Locate every Trypanosoma brucei.
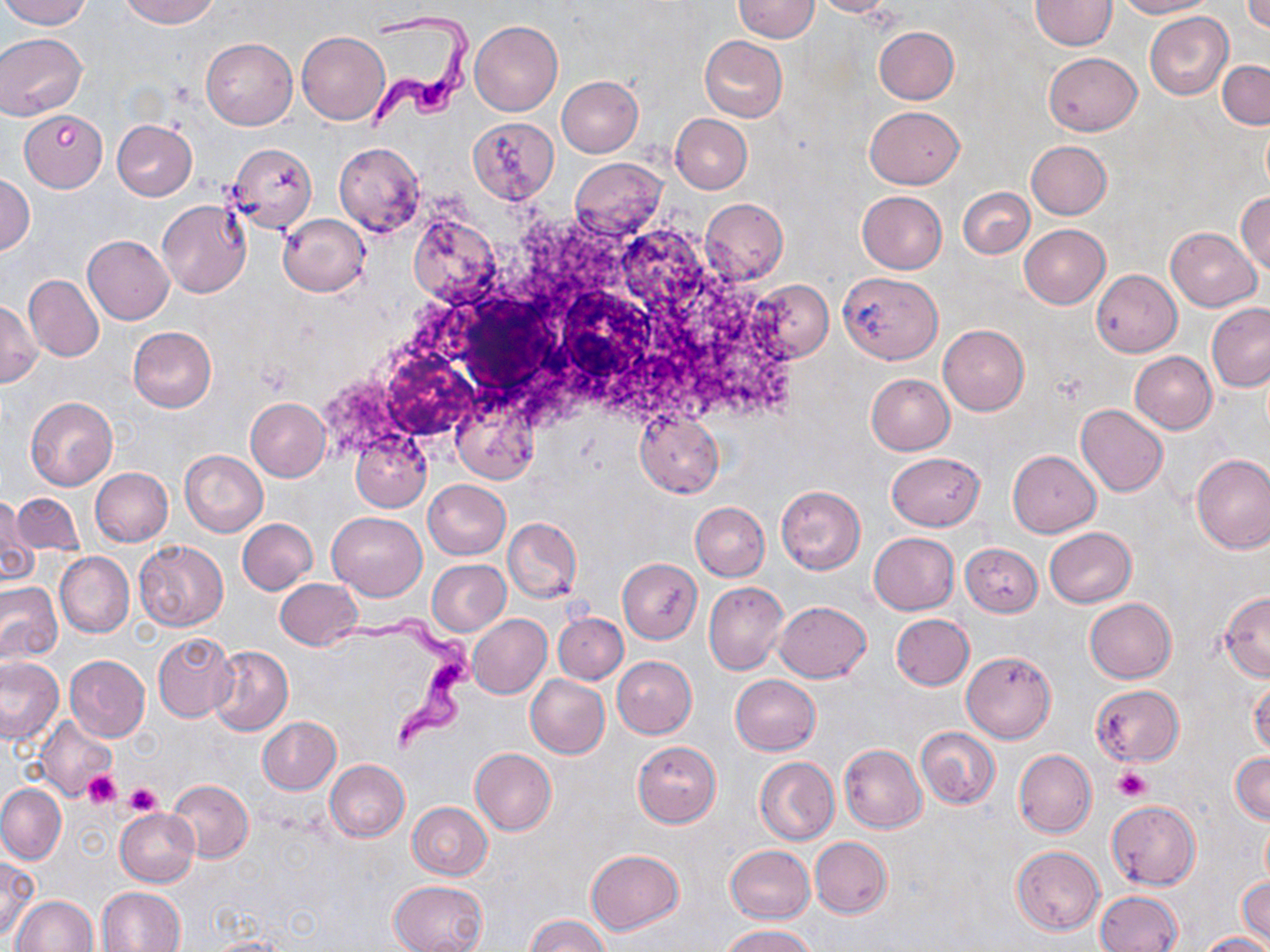

Approximate bounding boxes as (x1,y1)-(x2,y2) corner pairs in pixels.
Trypanosoma brucei: (362,12)-(474,131), (329,605)-(485,751).

Summary:
  - Platelet locations: (1114,766)-(1151,802), (82,771)-(123,808), (125,783)-(163,817)
  - Uninfected red blood cell locations: (3,0)-(91,29), (120,0)-(219,27), (732,0)-(821,42), (810,0)-(896,17), (1029,0)-(1117,51), (1116,0)-(1215,18), (1242,1)-(1270,33), (1144,12)-(1234,100), (470,21)-(563,116), (874,27)-(959,104), (297,30)-(390,125), (0,32)-(87,119), (699,35)-(788,121), (201,38)-(297,128), (1044,53)-(1141,135), (1217,59)-(1269,128), (556,76)-(643,157), (865,106)-(965,188), (19,110)-(108,191), (670,114)-(752,193), (467,116)-(559,205), (112,120)-(197,200), (1025,141)-(1111,219), (334,143)-(425,236), (227,144)-(317,233), (570,157)-(667,240), (1,173)-(35,256), (958,187)-(1033,258), (1235,191)-(1270,274), (856,192)-(947,274), (699,197)-(788,285), (156,201)-(251,298), (277,213)-(370,297), (408,214)-(501,304), (613,224)-(713,323), (1019,224)-(1110,309), (1165,227)-(1260,311), (84,236)-(174,324), (1091,269)-(1182,356), (838,271)-(944,362), (25,275)-(104,361), (749,279)-(833,361), (0,299)-(43,387), (1206,303)-(1270,390), (939,325)-(1029,415), (127,326)-(216,412), (1130,352)-(1217,433), (865,373)-(953,456), (451,395)-(539,484), (26,397)-(117,490), (246,397)-(331,481), (1076,404)-(1168,497), (634,411)-(723,498), (351,431)-(430,512), (180,450)-(268,535), (1008,450)-(1100,537), (886,452)-(985,531), (1191,454)-(1270,553), (90,467)-(173,547), (423,479)-(511,559), (775,486)-(865,573), (11,490)-(82,559), (1,495)-(36,586), (690,502)-(769,581), (327,512)-(427,600), (504,517)-(581,602), (237,518)-(318,595), (1044,527)-(1136,607), (869,533)-(960,614), (134,540)-(229,631), (960,543)-(1041,617), (55,552)-(134,638), (426,559)-(510,636), (617,559)-(702,643), (275,578)-(361,650), (0,582)-(62,664), (704,582)-(789,676), (1218,592)-(1270,681), (1084,598)-(1176,683), (773,601)-(872,682), (554,612)-(627,685), (467,614)-(552,699), (891,614)-(974,691), (152,632)-(238,723), (208,644)-(293,736), (960,650)-(1056,743), (64,655)-(150,742), (612,656)-(697,738), (0,657)-(66,746), (730,674)-(821,755), (525,675)-(609,759), (1248,676)-(1270,758), (1091,685)-(1184,766), (35,715)-(117,802), (257,717)-(340,795), (916,727)-(1000,809), (632,741)-(722,828), (839,745)-(927,833), (470,747)-(556,834), (1013,749)-(1096,839), (1231,752)-(1269,824), (754,756)-(839,845), (326,759)-(410,841), (167,779)-(253,862), (0,783)-(66,863), (407,801)-(492,879), (1106,801)-(1200,889), (115,808)-(200,887), (1261,818)-(1270,889), (810,837)-(893,918), (726,845)-(815,923), (1011,846)-(1105,934), (585,848)-(684,935), (0,856)-(37,940), (1238,876)-(1269,943), (389,880)-(488,952), (98,886)-(185,952), (1095,891)-(1182,952), (11,896)-(99,952), (525,914)-(609,952), (720,924)-(819,952), (1200,932)-(1269,952), (199,935)-(291,952)
  - Slide-level diagnosis: Trypanosoma brucei
  - Magnification: 1000x
  - Preparation: thin blood film
  - Modality: light microscopy
  - Field of view: one of a larger specimen
  - Stain: May-Grünwald-Giemsa
  - Image size: 1270×952 pixels